Assess the morphology of the erythrocytes.
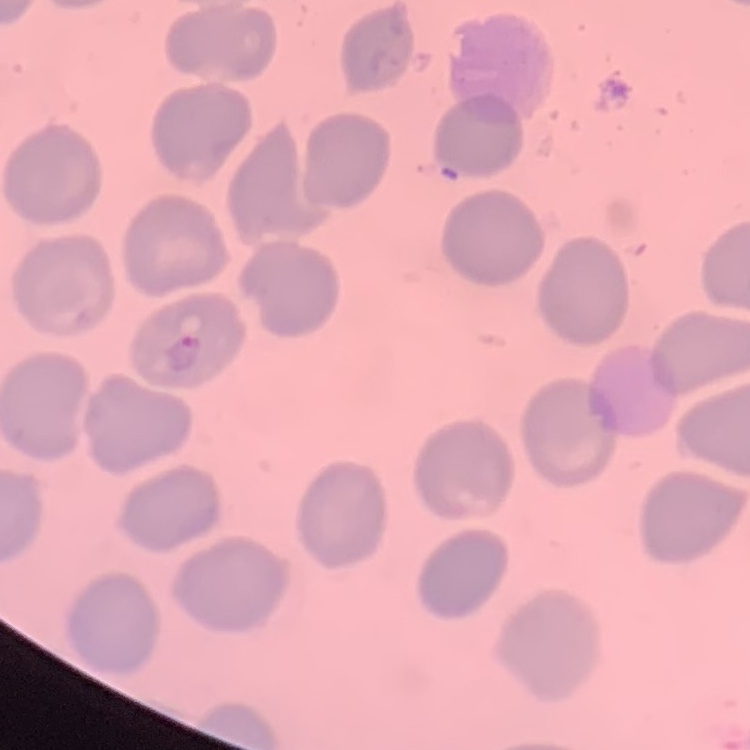
They show no rouleaux formation.

Thin blood smear. Stained with either Field's or Giemsa. Square crop of a larger photomicrograph.